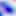

Toxoplasma gondii is seen. Photomicrograph. Captured at 400x magnification.